Assess this cell for malaria.
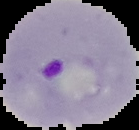

Parasitized.

From a thin blood film. Segmented cell region on a black background. Image is 139×130 pixels.